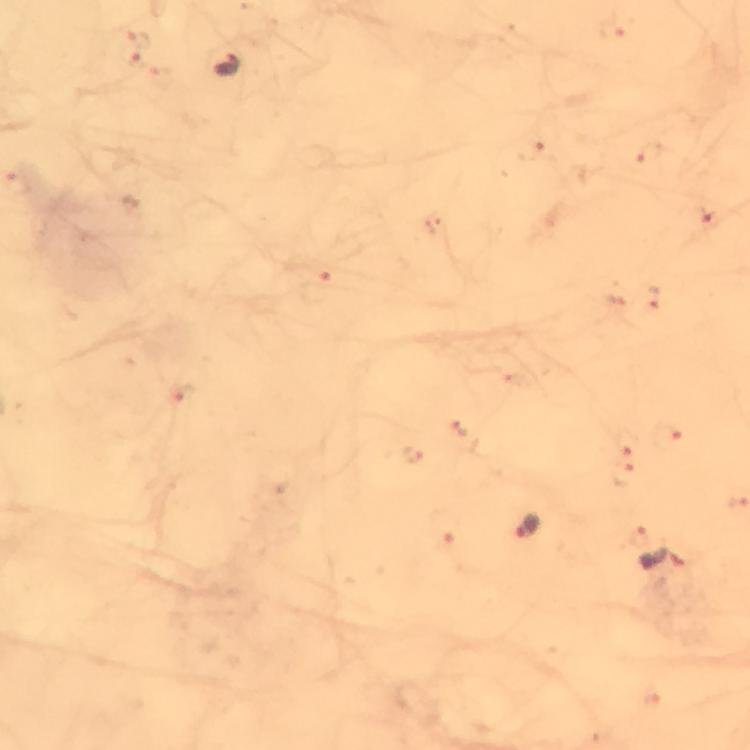

Approximate centers as (x, y) in pixels. Plasmodium parasite locations: (228, 67), (529, 528), (664, 562). Thick blood film. Immersion oil was used. Giemsa-stained preparation. From a malaria diagnostic workup. Image is 750×750 pixels. 100x magnification. Cropped region of a single field of view. Photographed with a smartphone mounted on the microscope.